Assess this cell for malaria.
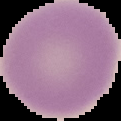
It is uninfected.

Summary:
  - Image type: segmented cell region on a black background
  - Image size: 121×121 pixels
  - Preparation: thin blood film